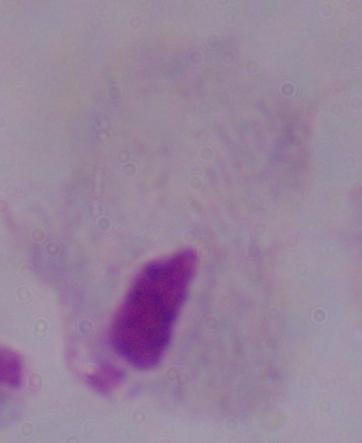
{
  "modality": "micrograph",
  "identification": "trichomonad",
  "magnification": "1000x"
}